Identify the cell.
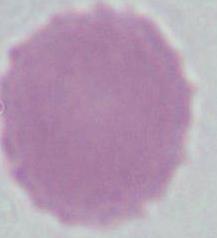
An erythrocyte.

Summary:
  - Modality: micrograph
  - Magnification: 1000x